Give the extent of all Plasmodium vivax-infected red blood cells.
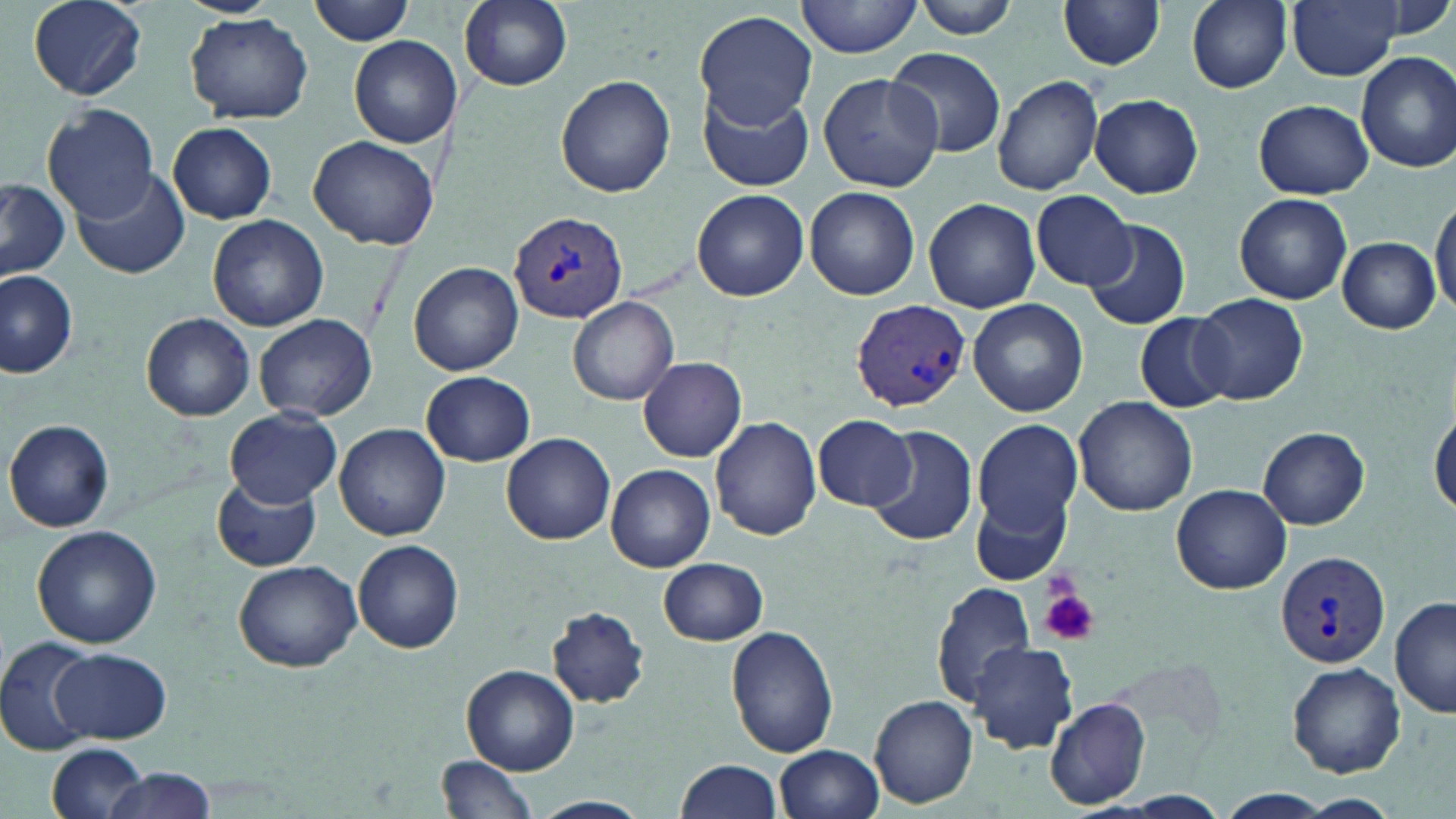

Approximate bounding boxes as (x1,y1)-(x2,y2) corner pairs in pixels.
Plasmodium vivax-infected red blood cells: (511,210)-(626,322), (849,300)-(971,412), (1275,549)-(1391,669).

Platelet locations: (1039,586)-(1097,646). Uninfected red blood cell locations: (26,0)-(150,100), (175,0)-(283,17), (309,0)-(415,45), (458,0)-(572,90), (796,0)-(920,58), (910,0)-(1021,39), (1185,0)-(1292,92), (1287,0)-(1406,81), (1058,1)-(1166,72), (695,9)-(817,129), (185,13)-(314,123), (349,35)-(463,148), (884,46)-(1008,158), (1354,50)-(1456,173), (816,71)-(943,192), (556,74)-(677,197), (992,75)-(1105,194), (698,86)-(812,193), (1090,95)-(1203,198), (1252,98)-(1373,199), (42,104)-(161,220), (168,122)-(277,223), (308,135)-(441,250), (74,170)-(190,280), (0,183)-(70,280), (804,186)-(919,301), (692,188)-(809,301), (1030,189)-(1136,289), (1234,193)-(1353,305), (1431,193)-(1456,319), (925,197)-(1040,313), (207,214)-(328,331), (1083,218)-(1190,329), (1336,236)-(1439,334), (409,261)-(523,375), (1,270)-(78,377), (1194,294)-(1307,403), (570,296)-(680,404), (969,298)-(1089,418), (1133,312)-(1238,413), (141,314)-(256,420), (254,314)-(377,422), (638,357)-(747,462), (421,371)-(535,466), (1072,397)-(1198,516), (226,408)-(342,507), (1429,408)-(1456,519), (813,414)-(915,510), (710,415)-(822,541), (970,417)-(1082,538), (4,419)-(115,533), (335,423)-(451,542), (868,426)-(978,550), (1257,426)-(1371,529), (502,433)-(615,544), (607,463)-(715,572), (211,478)-(323,571), (1171,483)-(1293,595), (970,489)-(1072,588), (32,526)-(163,647), (353,539)-(463,653), (659,557)-(768,646), (234,560)-(360,673), (931,581)-(1038,708), (1391,597)-(1455,720), (546,606)-(651,708), (726,625)-(837,758), (1,636)-(99,757), (969,641)-(1079,754), (53,648)-(170,742), (1288,662)-(1406,777), (462,664)-(579,775), (868,694)-(979,809), (1044,695)-(1151,809), (46,743)-(152,819), (776,745)-(885,819), (438,756)-(538,819), (675,757)-(784,819), (97,769)-(220,819), (1212,790)-(1334,819), (532,794)-(651,817), (1300,796)-(1400,816). Slide-level diagnosis: Plasmodium vivax. May-Grünwald-Giemsa-stained preparation. Captured at 1000x magnification. Thin blood film. Image is 1456×819 pixels. Light microscopy. Single field of view.